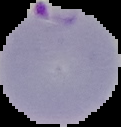
The area outside the segmented cell region is set to black. From a thin blood film. Result: Plasmodium parasites detected. Image is 121×127 pixels.